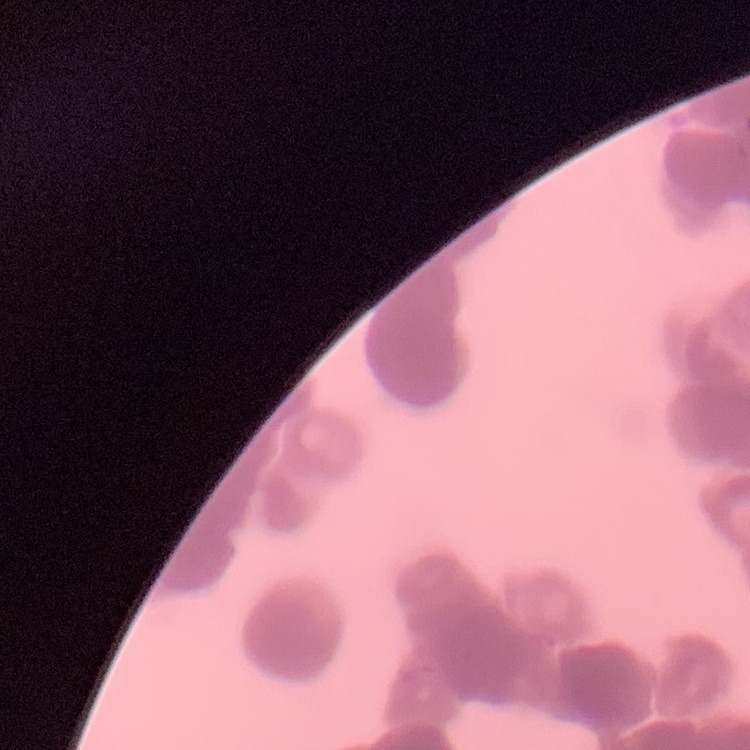 The red blood cells show rouleaux formation. One tile cut from a larger photomicrograph. Thin blood smear. Stained with either Field's or Giemsa.